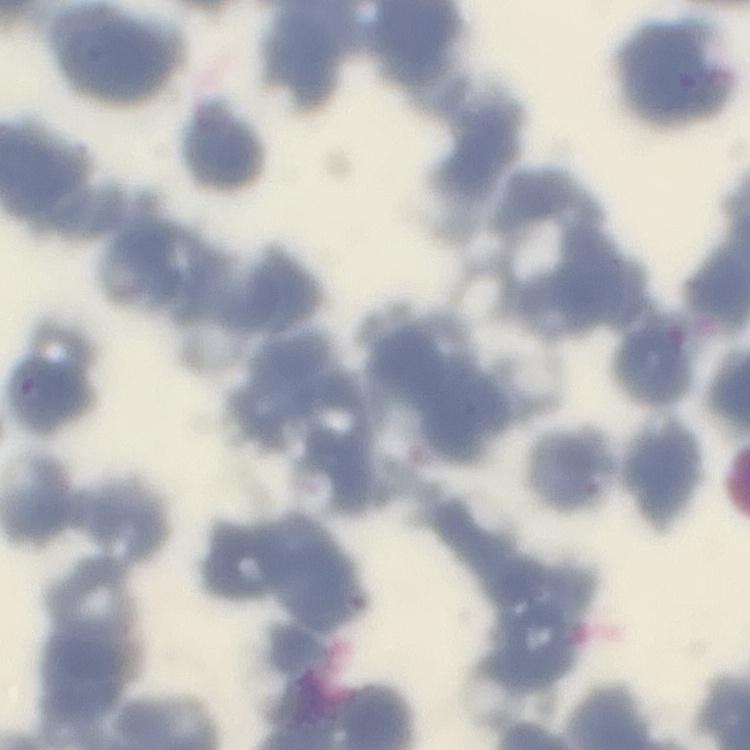
The red blood cells show rouleaux formation. Square crop of a larger photomicrograph. Thin peripheral smear. Stained with either Field's or Giemsa.